Report the malaria status of this cell.
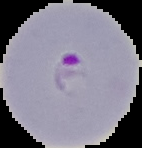

It is parasitized.

Summary:
  - Preparation: thin blood smear
  - Image type: segmented cell region with the area outside set to black
  - Image size: 142×148 pixels